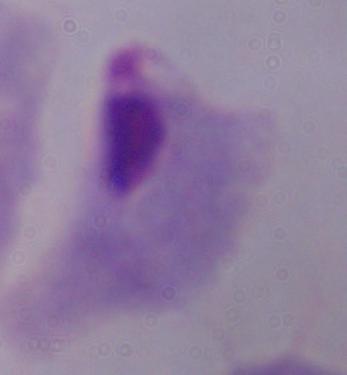
identification = trichomonad
modality = micrograph
magnification = 1000x